Locate every Plasmodium parasite.
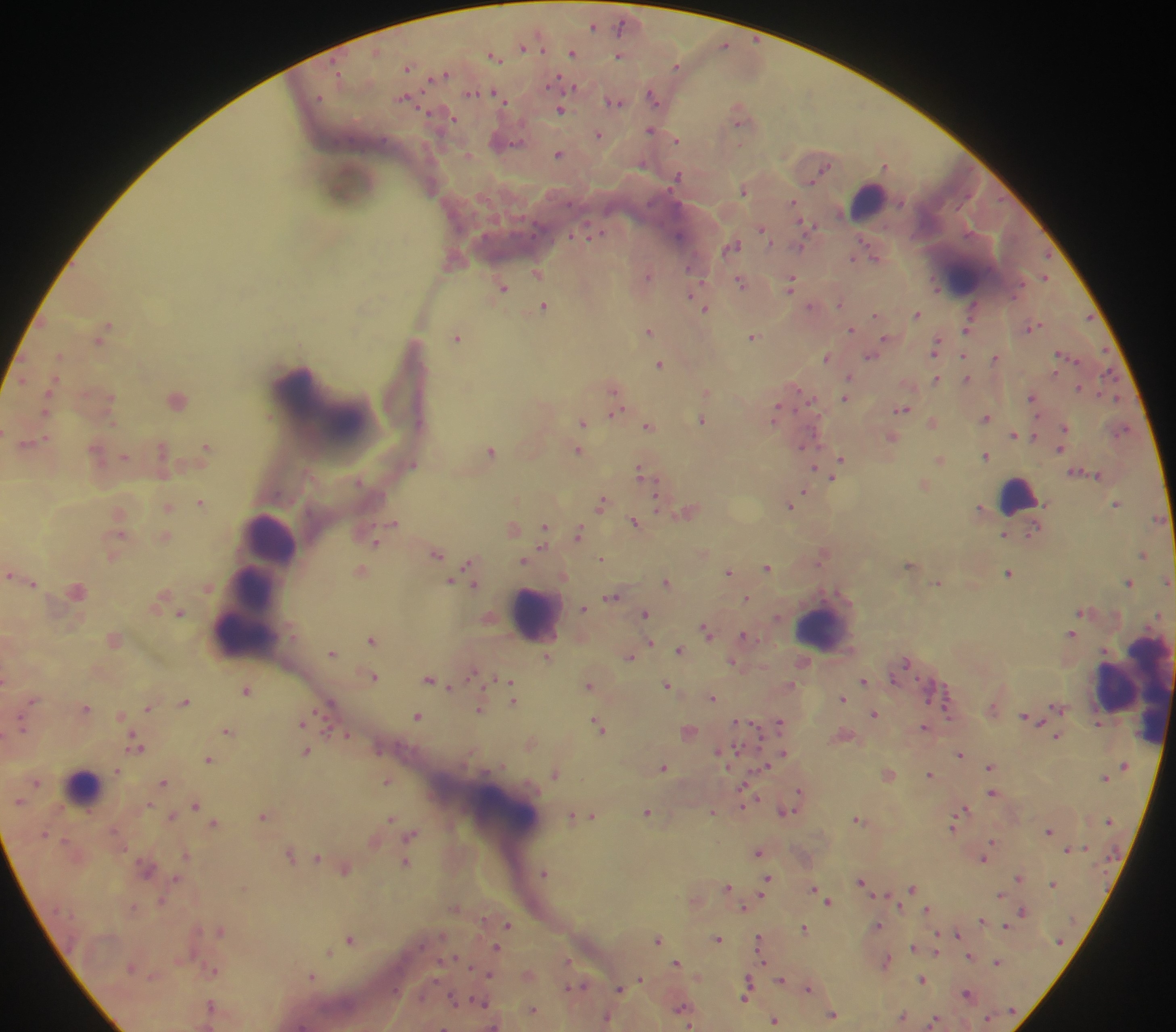
Approximate centers as [x, y] in pixels.
Plasmodium parasites: [621, 23], [592, 26], [724, 44], [523, 47], [543, 49], [572, 53], [619, 55], [678, 65], [337, 67], [410, 67], [443, 73], [556, 81], [564, 83], [575, 87], [472, 93], [653, 97], [407, 98], [504, 98], [616, 100], [565, 101], [561, 110], [448, 117], [738, 123], [652, 129], [599, 135], [678, 139], [508, 141], [560, 153], [886, 165], [825, 167], [679, 175], [812, 183], [744, 191], [792, 200], [803, 223], [595, 233], [765, 233], [571, 236], [407, 238], [768, 239], [862, 239], [734, 244], [1046, 254], [876, 257], [853, 258], [688, 269], [536, 272], [649, 275], [1044, 277], [791, 279], [740, 282], [702, 284], [504, 287], [698, 288], [935, 288], [691, 297], [810, 305], [543, 306], [707, 308], [917, 313], [875, 314], [109, 324], [851, 327], [650, 330], [966, 330], [755, 334], [459, 336], [884, 336], [1061, 353], [871, 356], [964, 356], [826, 357], [995, 358], [1074, 359], [658, 364], [1106, 370], [1056, 372], [849, 376], [1104, 376], [966, 378], [937, 379], [1077, 388], [614, 390], [1098, 392], [1032, 396], [174, 397], [810, 397], [845, 398], [778, 408], [904, 409], [614, 414], [700, 420], [582, 422], [647, 423], [813, 428], [1066, 428], [1014, 435], [1034, 437], [1062, 448], [577, 449], [492, 451], [987, 455], [841, 459], [939, 460], [415, 464], [813, 467], [639, 469], [832, 478], [657, 479], [805, 490], [659, 496], [602, 500], [199, 503], [1118, 503], [657, 505], [791, 507], [119, 511], [655, 512], [635, 521], [394, 522], [546, 525], [578, 534], [379, 537], [377, 543], [543, 547], [436, 554], [601, 558], [524, 562], [468, 565], [768, 567], [361, 569], [729, 570], [10, 573], [1009, 575], [450, 582], [667, 582], [1128, 582], [34, 583], [475, 584], [611, 596], [746, 598], [584, 608], [645, 613], [777, 618], [705, 629], [1072, 630], [743, 636], [371, 639], [651, 642], [680, 651], [332, 653], [630, 657], [907, 664], [473, 672], [374, 677], [494, 678], [431, 679], [5, 681], [511, 684], [667, 685], [590, 686], [449, 687], [246, 690], [713, 698], [34, 699], [515, 701], [332, 703], [86, 708], [148, 709], [949, 710], [317, 711], [481, 711], [122, 714], [874, 714], [419, 716], [779, 720], [736, 721], [597, 724], [301, 725], [922, 726], [23, 728], [228, 730], [132, 733], [327, 733], [1056, 735], [348, 736], [140, 748], [737, 748], [306, 751], [717, 751], [379, 753], [783, 754], [958, 756], [209, 759], [989, 769], [119, 770], [555, 773], [931, 775], [1105, 777], [164, 783], [37, 784], [386, 784], [739, 788], [799, 789], [991, 793], [19, 801], [149, 805], [196, 806], [742, 806], [966, 808], [796, 811], [646, 812], [172, 815], [572, 815], [593, 815], [263, 816], [392, 819], [215, 823], [1108, 823], [953, 829], [1048, 832], [413, 833], [46, 834], [408, 839], [994, 841], [758, 853], [185, 856], [319, 859], [983, 859], [406, 863], [147, 868], [546, 872], [768, 877], [1018, 877], [176, 879], [861, 879], [1051, 884], [727, 887], [812, 888], [913, 888], [760, 894], [1002, 894], [873, 895], [163, 900], [828, 902], [135, 906], [743, 908], [926, 910], [1022, 910], [981, 920], [508, 924], [879, 925], [1004, 926], [803, 927], [220, 932], [937, 933], [957, 933], [758, 936], [718, 938], [349, 939], [658, 940], [492, 946], [913, 947], [329, 952], [762, 960], [997, 960], [567, 961], [677, 961], [214, 971], [748, 977], [641, 978], [781, 978], [921, 979], [568, 986], [620, 989], [807, 989], [966, 993], [744, 998], [209, 1003], [478, 1004], [680, 1007], [833, 1015], [774, 1021], [690, 1026].

{
  "field_of_view": "single",
  "leukocyte_locations": "approximate centers as [x, y] in pixels: [871, 204], [1019, 497], [269, 535], [254, 592], [538, 616], [825, 631], [241, 644], [1117, 689], [1149, 689], [85, 785], [502, 809]",
  "capture": "mobile-phone photograph through a microscope",
  "country": "Ghana",
  "preparation": "thick blood smear",
  "image_size": "1176×1032 pixels"
}